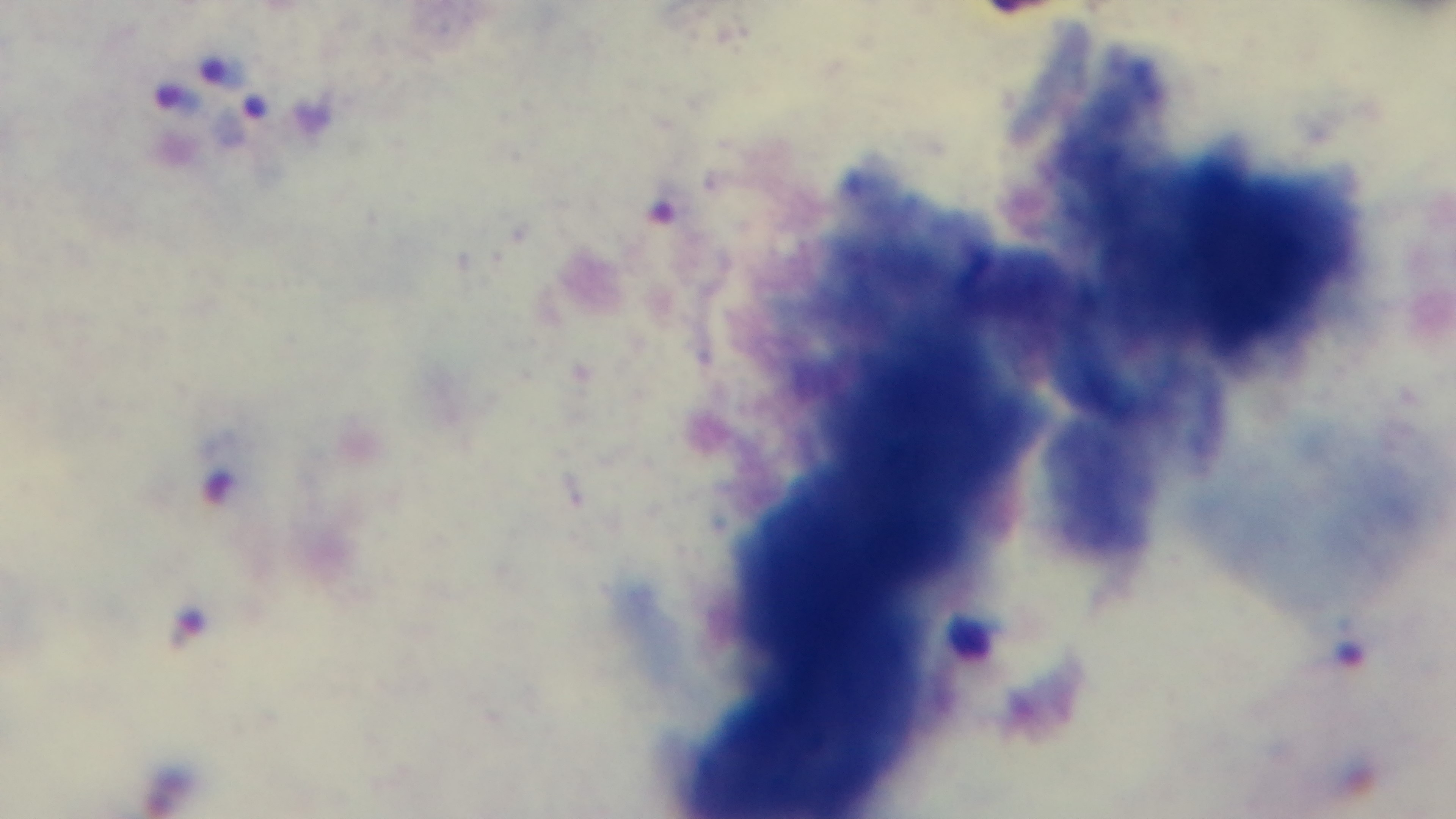
Mounted 4K digital camera. Single field of view. Oil-immersion objective, 100x. Light microscopy. Giemsa stain. Preparation: thick blood film. Malaria status: positive.